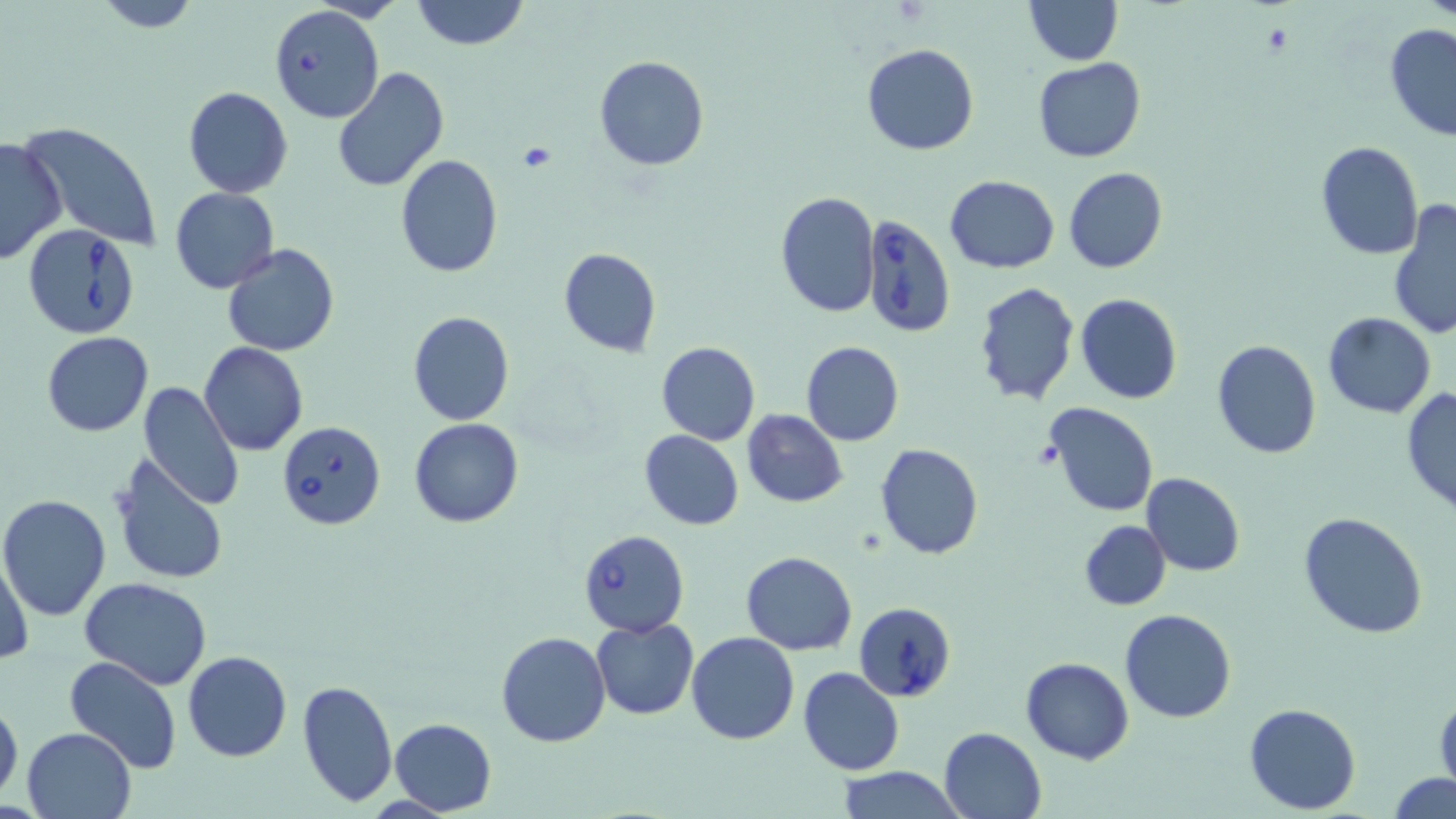

Summary:
  - Coordinate format: approximate bounding boxes as [x1, y1, x2, y2] in pixels
  - Platelet locations: [518, 143, 557, 174]
  - Uninfected red blood cell locations: [412, 0, 528, 50], [1024, 0, 1122, 65], [92, 1, 202, 31], [1382, 22, 1456, 143], [862, 44, 979, 155], [593, 55, 708, 171], [1032, 57, 1145, 163], [332, 67, 449, 193], [185, 86, 293, 198], [18, 122, 162, 252], [0, 136, 66, 267], [1314, 141, 1425, 259], [395, 154, 503, 278], [1063, 166, 1168, 274], [944, 175, 1061, 273], [170, 186, 280, 293], [774, 191, 880, 318], [1387, 198, 1456, 340], [223, 244, 340, 356], [558, 248, 660, 357], [973, 282, 1079, 406], [1075, 292, 1183, 404], [407, 310, 515, 427], [1323, 311, 1436, 419], [42, 331, 153, 436], [1210, 339, 1323, 458], [801, 340, 905, 447], [656, 341, 761, 445], [200, 343, 308, 456], [139, 381, 242, 514], [1400, 387, 1456, 518], [1046, 404, 1158, 517], [741, 409, 848, 508], [408, 418, 523, 528], [640, 429, 744, 529], [874, 443, 984, 560], [111, 455, 230, 587], [1141, 472, 1246, 576], [0, 494, 111, 619], [1298, 511, 1430, 640], [1079, 520, 1171, 611], [0, 548, 33, 666], [740, 552, 857, 655], [81, 577, 213, 689], [1119, 609, 1237, 724], [591, 618, 699, 720], [497, 631, 610, 747], [686, 631, 800, 745], [183, 651, 292, 762], [64, 656, 183, 775], [1020, 657, 1134, 765], [798, 666, 905, 776], [297, 679, 397, 808], [1434, 693, 1456, 799], [0, 698, 23, 807], [1245, 702, 1361, 814], [389, 718, 497, 814], [21, 726, 137, 819], [939, 726, 1047, 819], [835, 767, 965, 819], [1389, 772, 1456, 817]
  - Babesia divergens-infected red blood cell locations: [267, 4, 385, 124], [861, 212, 958, 337], [22, 224, 141, 341], [276, 419, 387, 529], [579, 529, 688, 638], [853, 601, 958, 702]
  - Slide-level diagnosis: Babesia divergens
  - Modality: optical microscopy
  - Magnification: 1000x
  - Image size: 1456×819 pixels
  - Field of view: one of a larger specimen
  - Preparation: thin blood film
  - Stain: May-Grünwald-Giemsa